Describe the morphology of the red blood cells.
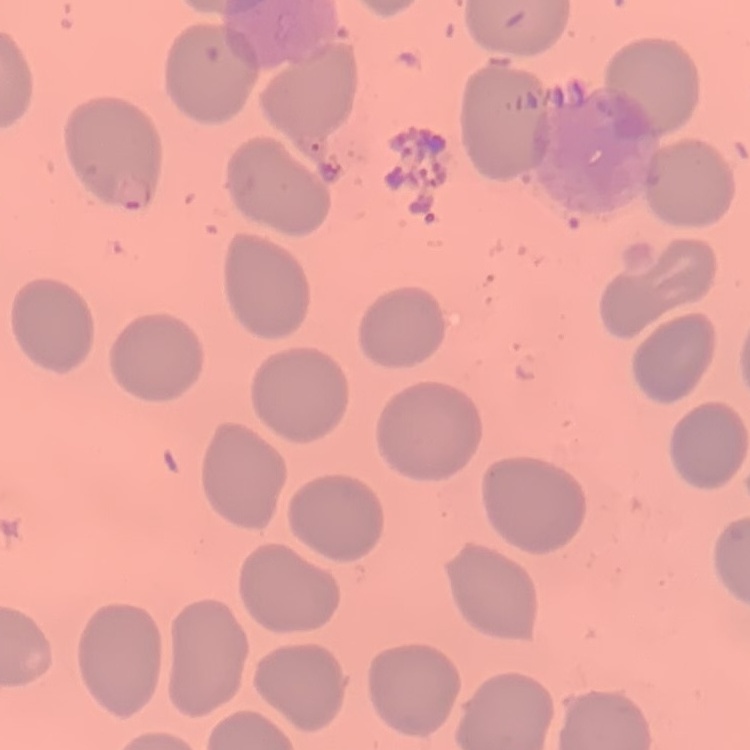
They show no rouleaux formation.

Stained with either Field's or Giemsa. Thin blood film. Square crop of a larger photomicrograph.